State which parasite is depicted.
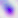

Toxoplasma gondii.

modality = micrograph
magnification = 400x